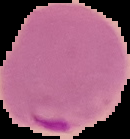

{
  "result": "Plasmodium parasites detected",
  "image_size": "130×139 pixels",
  "preparation": "thin blood smear",
  "image_type": "cell region segmented out of the field of view; surrounding area masked to black"
}